Give the extent of all Plasmodium falciparum-infected red blood cells.
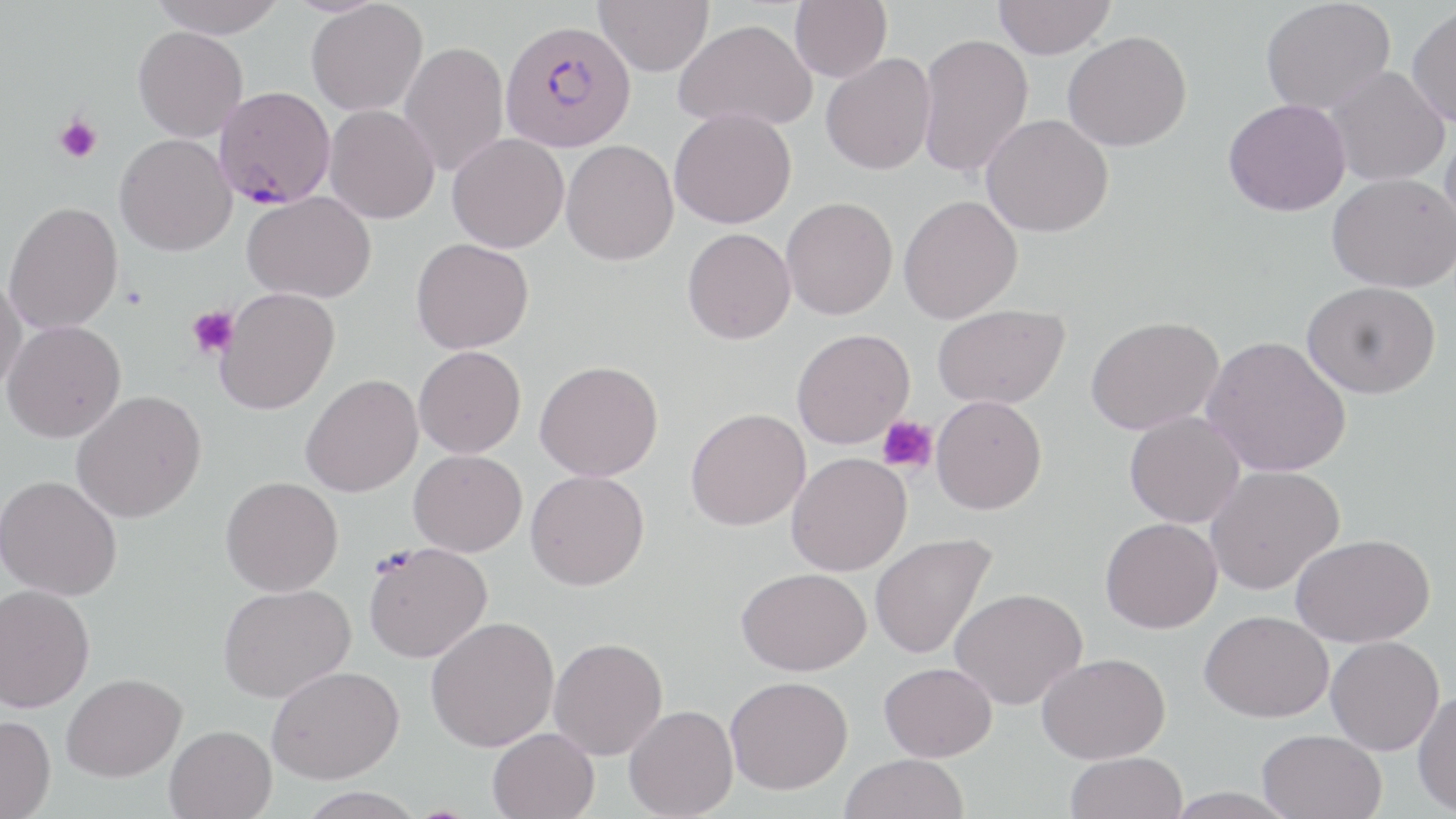
Approximate bounding boxes as [x1, y1, x2, y2] in pixels.
Plasmodium falciparum-infected red blood cells: [501, 20, 636, 152], [214, 86, 336, 209].

{
  "slide_level_diagnosis": "Plasmodium falciparum",
  "platelet_locations": "approximate bounding boxes as [x1, y1, x2, y2] in pixels: [54, 115, 102, 164], [186, 304, 238, 360], [876, 415, 938, 473]",
  "image_size": "1456×819 pixels",
  "preparation": "thin blood smear",
  "stain": "May-Grünwald-Giemsa",
  "uninfected_red_blood_cell_locations": "approximate bounding boxes as [x1, y1, x2, y2] in pixels: [149, 0, 286, 38], [594, 0, 714, 76], [789, 0, 892, 83], [1260, 0, 1395, 115], [305, 1, 428, 116], [993, 1, 1116, 59], [1407, 5, 1456, 128], [674, 18, 817, 132], [133, 26, 248, 142], [1062, 30, 1192, 151], [917, 32, 1034, 179], [399, 41, 509, 177], [820, 53, 936, 175], [1323, 65, 1449, 187], [1223, 98, 1351, 216], [324, 104, 440, 224], [669, 107, 796, 229], [981, 113, 1114, 237], [1440, 121, 1456, 243], [114, 133, 237, 256], [447, 133, 568, 253], [561, 140, 679, 266], [1326, 173, 1455, 292], [242, 191, 376, 303], [898, 195, 1022, 323], [781, 196, 898, 320], [3, 201, 124, 335], [682, 228, 795, 344], [411, 238, 534, 353], [0, 273, 27, 397], [1301, 281, 1441, 397], [214, 286, 339, 415], [932, 304, 1069, 409], [1085, 315, 1224, 436], [1, 320, 126, 442], [791, 328, 915, 448], [1201, 335, 1351, 477], [414, 346, 526, 457], [535, 359, 663, 481], [300, 373, 423, 497], [72, 390, 207, 523], [931, 395, 1047, 514], [685, 408, 810, 531], [1124, 411, 1245, 528], [409, 449, 527, 556], [786, 452, 912, 576], [1205, 465, 1344, 595], [525, 469, 649, 590], [0, 475, 122, 600], [221, 476, 343, 596], [1100, 517, 1222, 633], [869, 532, 997, 660], [1290, 533, 1434, 647], [363, 541, 492, 663], [736, 567, 870, 675], [218, 583, 355, 703], [0, 584, 94, 713], [949, 587, 1088, 710], [1200, 610, 1334, 722], [425, 616, 559, 752], [1325, 635, 1444, 755], [549, 637, 668, 759], [1037, 652, 1170, 764], [879, 661, 997, 761], [266, 665, 404, 784], [62, 672, 186, 782], [726, 676, 853, 794], [1412, 689, 1456, 815], [624, 705, 738, 818], [0, 714, 56, 818], [165, 724, 276, 819], [487, 727, 599, 819], [1257, 729, 1387, 818], [1065, 751, 1188, 819], [839, 754, 969, 819], [298, 787, 426, 819], [1163, 787, 1300, 818]",
  "modality": "light microscopy",
  "magnification": "1000x",
  "field_of_view": "single"
}